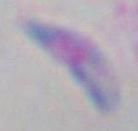
Summary:
  - Modality: micrograph
  - Identification: Toxoplasma gondii
  - Magnification: 1000x